Give the position of every Plasmodium parasite visible.
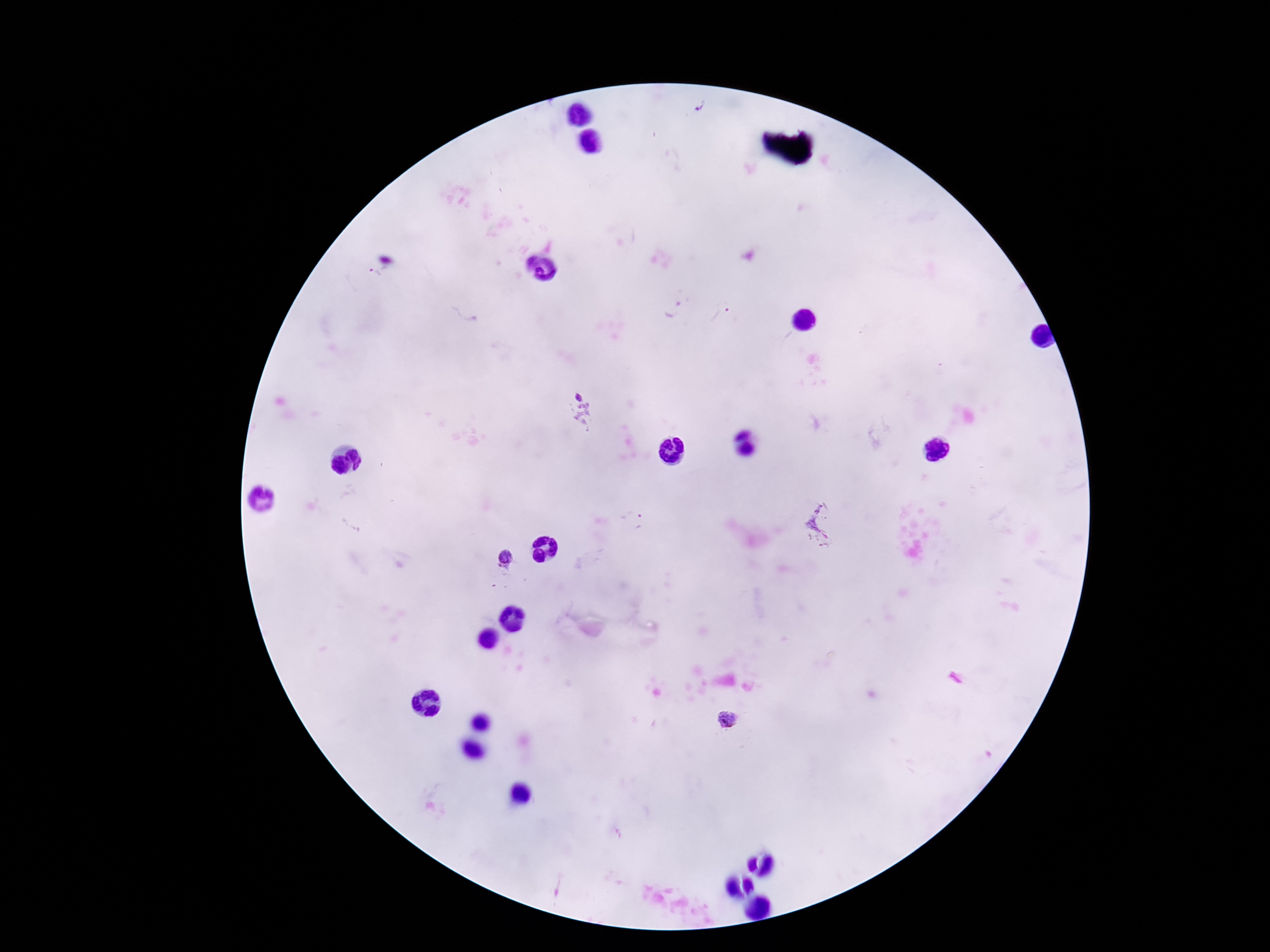
Approximate object centers, in pixels from the top-left corner.
Plasmodium parasites: (x=700, y=107), (x=674, y=309), (x=720, y=314), (x=581, y=410), (x=640, y=523), (x=827, y=525), (x=505, y=560), (x=728, y=719).

Image is 1270×952 pixels. 100x magnification. Thick blood film. Giemsa-stained preparation. Patient malaria status: infected. Single field of view. Smartphone photograph taken through the microscope eyepiece.